Give a bounding box for every Plasmodium parasite.
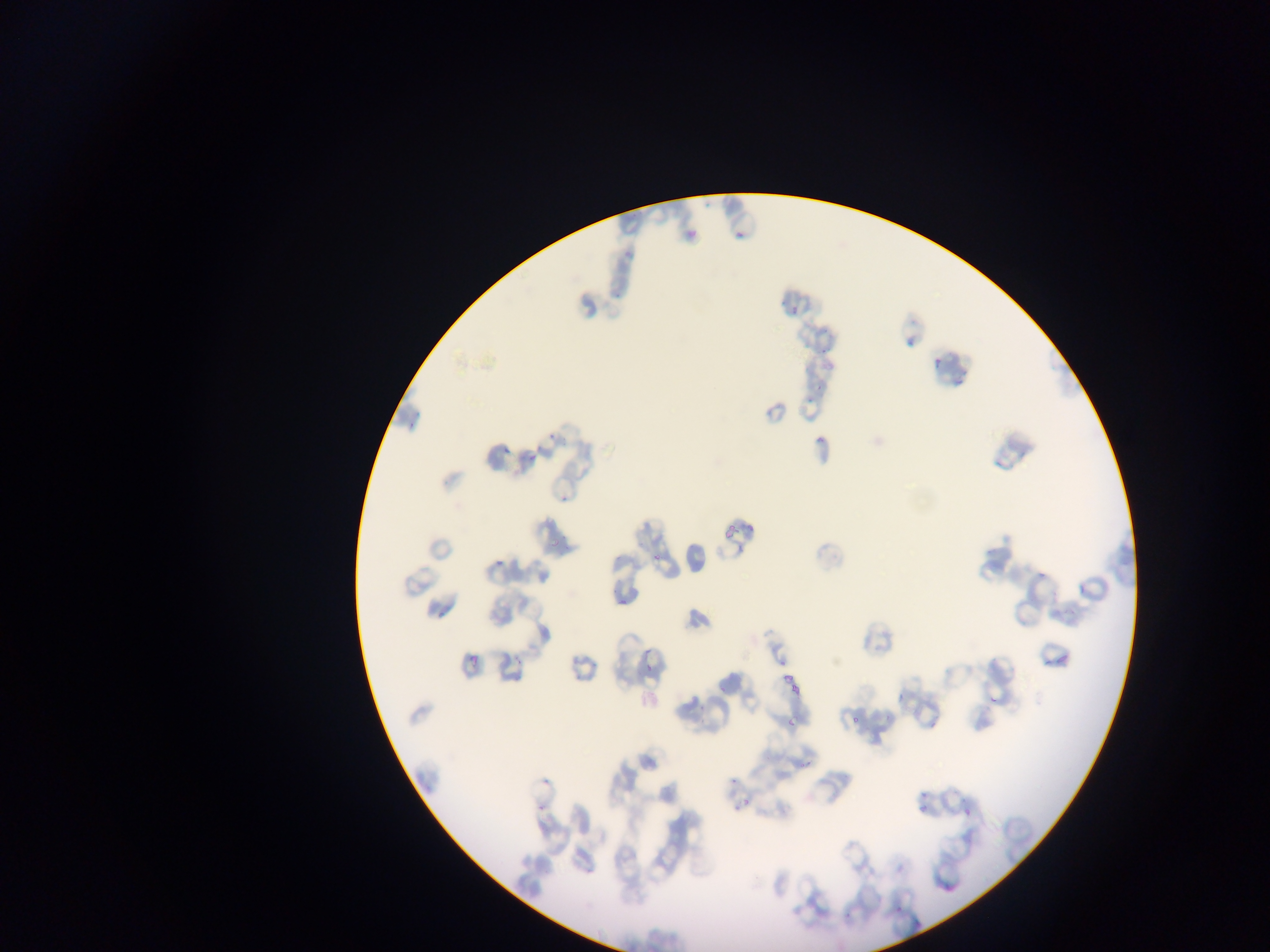
Approximate bounding boxes as {left, top, right, bottom} in pixels.
Plasmodium parasites: {732, 222, 749, 239}, {679, 227, 702, 243}, {622, 238, 643, 262}, {780, 300, 789, 310}, {791, 307, 804, 317}, {814, 328, 832, 338}, {817, 346, 830, 357}, {931, 352, 944, 369}, {953, 367, 971, 384}, {813, 377, 824, 396}, {803, 397, 815, 408}, {547, 431, 559, 448}, {815, 431, 827, 444}, {499, 440, 518, 457}, {528, 448, 543, 463}, {560, 489, 571, 504}, {717, 520, 742, 538}, {550, 536, 563, 549}, {650, 545, 663, 564}, {492, 553, 508, 567}, {1040, 562, 1055, 579}, {611, 592, 627, 611}, {1049, 644, 1068, 667}, {466, 647, 485, 665}, {1046, 651, 1053, 667}, {511, 652, 519, 663}, {643, 660, 655, 677}, {780, 670, 794, 685}, {785, 684, 800, 697}, {989, 684, 1008, 703}, {894, 686, 910, 700}, {784, 709, 803, 732}, {849, 713, 863, 724}, {795, 757, 812, 774}, {726, 773, 736, 784}, {540, 777, 551, 787}, {920, 786, 928, 803}, {739, 795, 753, 808}, {913, 800, 927, 813}, {731, 803, 740, 816}, {536, 804, 548, 813}, {963, 810, 972, 815}, {896, 903, 906, 910}, {841, 905, 859, 919}.

Summary:
  - Field of view: single
  - Image size: 1270×952 pixels
  - Preparation: thin blood film
  - Capture: mobile-phone photograph through a microscope
  - Country: Ghana